Locate every uninfected red blood cell.
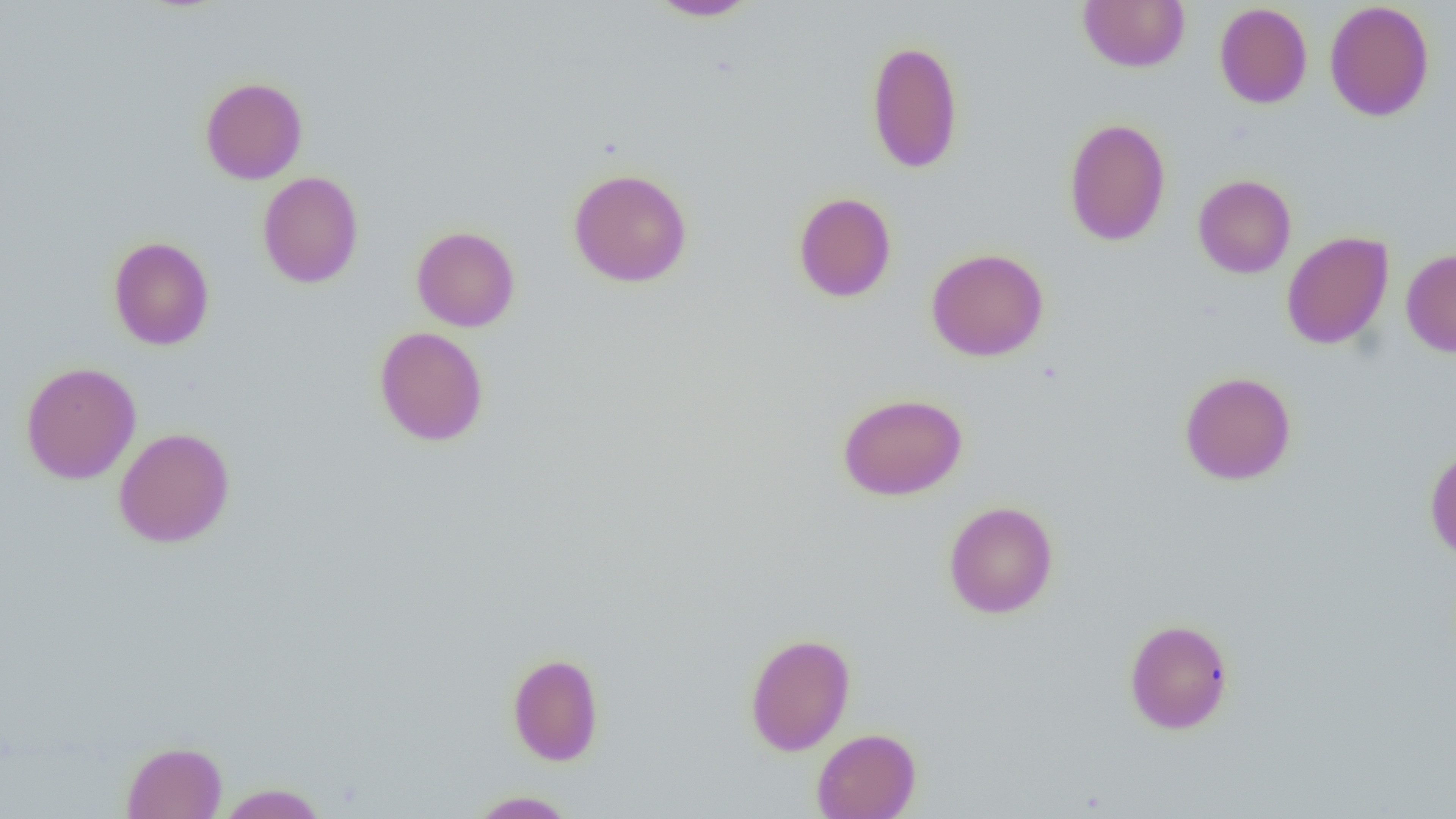

Approximate bounding boxes as (x1,y1)-(x2,y2) corner pairs in pixels.
Uninfected red blood cells: (1077,0)-(1190,73), (646,1)-(760,21), (1324,1)-(1435,122), (1214,2)-(1313,108), (866,39)-(964,174), (200,77)-(308,184), (1064,118)-(1171,247), (568,168)-(693,287), (257,171)-(364,288), (1193,174)-(1296,278), (793,192)-(897,302), (411,225)-(520,332), (1281,231)-(1394,350), (108,236)-(215,350), (926,248)-(1049,361), (1401,248)-(1456,357), (374,326)-(489,446), (20,361)-(141,485), (1179,371)-(1297,485), (838,393)-(967,500), (113,427)-(235,548), (1424,444)-(1456,561), (942,500)-(1058,619), (1124,618)-(1234,734), (744,632)-(855,756), (507,652)-(604,766), (812,728)-(921,819), (121,741)-(227,819), (216,783)-(329,818), (467,790)-(578,818).

Summary:
  - Slide-level diagnosis: negative for blood parasites
  - Magnification: 1000x
  - Image size: 1456×819 pixels
  - Modality: optical microscopy
  - Preparation: thin blood smear
  - Field of view: one of a larger specimen